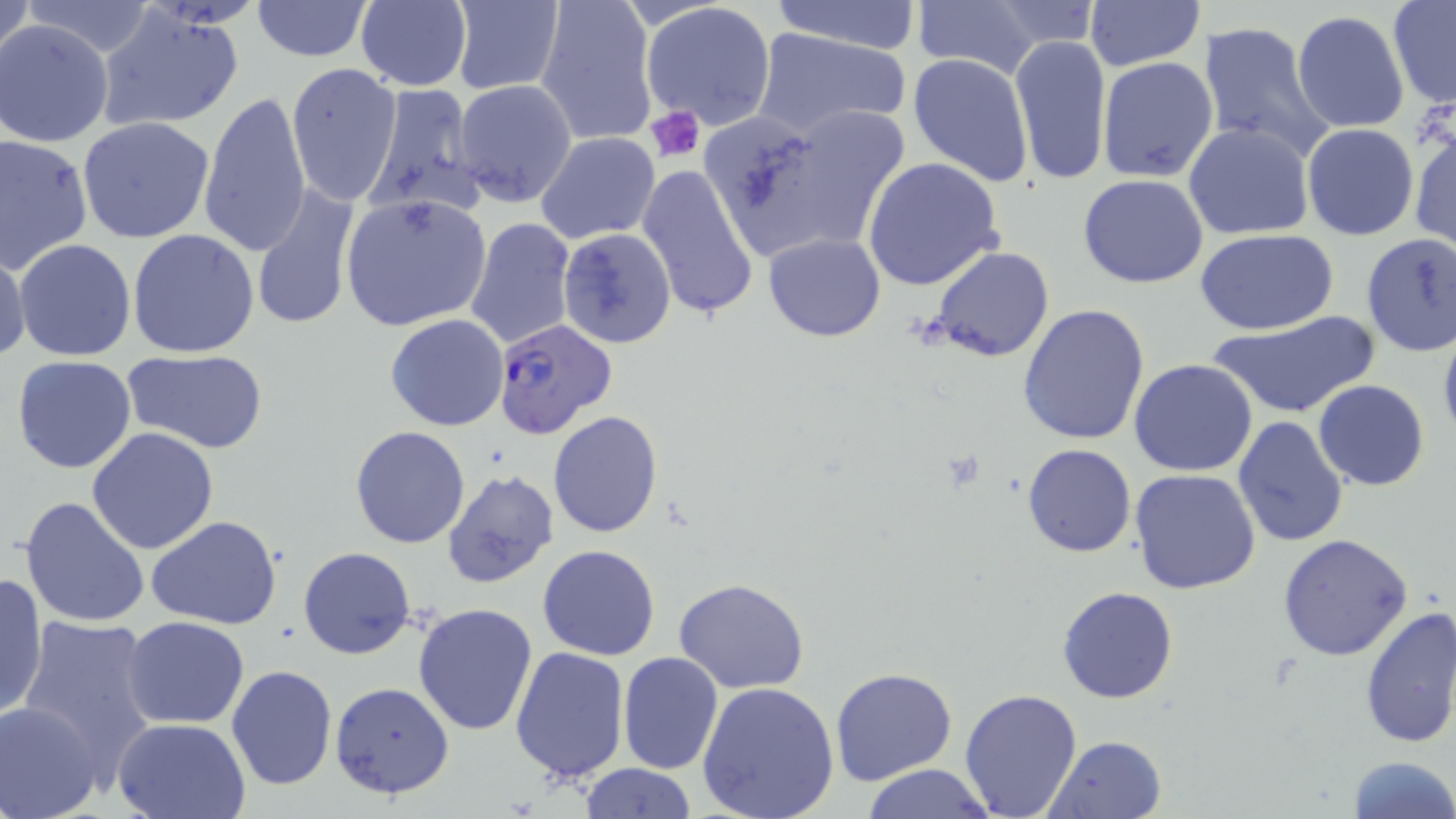

Approximate bounding boxes as [x1, y1, x2, y2] in pixels. Plasmodium falciparum-infected red blood cell locations: [493, 319, 620, 441]. Uninfected red blood cell locations: [19, 0, 156, 58], [762, 0, 925, 54], [1083, 0, 1202, 71], [1, 1, 34, 65], [249, 1, 375, 61], [449, 1, 565, 95], [534, 1, 657, 146], [909, 1, 1044, 81], [355, 2, 472, 90], [641, 2, 778, 132], [1387, 2, 1456, 109], [984, 3, 1106, 51], [96, 7, 247, 132], [1293, 10, 1411, 135], [1, 20, 113, 147], [1198, 22, 1337, 164], [750, 26, 914, 141], [1009, 35, 1112, 184], [1026, 48, 1189, 182], [908, 54, 1035, 185], [1097, 56, 1219, 183], [287, 63, 401, 204], [453, 79, 577, 207], [363, 83, 483, 217], [200, 91, 312, 257], [721, 105, 913, 265], [1408, 116, 1455, 255], [77, 117, 218, 245], [1184, 122, 1314, 240], [1302, 122, 1418, 241], [535, 132, 661, 245], [1, 134, 94, 273], [862, 156, 1006, 292], [636, 163, 761, 321], [1079, 174, 1209, 289], [250, 184, 362, 332], [340, 195, 492, 331], [463, 216, 577, 352], [128, 228, 260, 358], [557, 228, 676, 349], [1195, 229, 1340, 335], [764, 232, 885, 342], [1358, 234, 1456, 357], [12, 239, 137, 361], [0, 245, 29, 366], [929, 246, 1055, 364], [1018, 304, 1151, 447], [1205, 309, 1378, 421], [385, 314, 510, 431], [1436, 323, 1456, 452], [123, 349, 270, 453], [11, 354, 138, 474], [1129, 359, 1259, 476], [1313, 379, 1430, 491], [548, 411, 663, 538], [1233, 417, 1349, 546], [350, 426, 471, 549], [86, 427, 221, 554], [1022, 443, 1135, 559], [442, 469, 559, 588], [1131, 469, 1262, 593], [20, 495, 151, 629], [147, 516, 282, 627], [1277, 533, 1417, 663], [537, 544, 661, 660], [299, 546, 415, 659], [0, 572, 49, 721], [673, 576, 810, 693], [1057, 586, 1179, 704], [412, 602, 540, 736], [1358, 605, 1456, 749], [15, 613, 161, 779], [123, 616, 250, 728], [171, 636, 321, 776], [508, 646, 631, 783], [618, 652, 723, 774], [226, 664, 337, 790], [831, 667, 959, 787], [329, 681, 456, 799], [697, 681, 840, 819], [958, 688, 1084, 818], [0, 700, 104, 819], [113, 718, 251, 819], [1046, 733, 1168, 819], [1346, 755, 1455, 819], [576, 763, 696, 818], [859, 764, 998, 819]. Platelet locations: [647, 106, 706, 162]. Slide-level diagnosis: Plasmodium falciparum. Captured at 1000x magnification. Thin blood smear. May-Grünwald-Giemsa-stained preparation. Image is 1456×819 pixels. One field of a larger specimen. Light microscopy.